Identify the parasite.
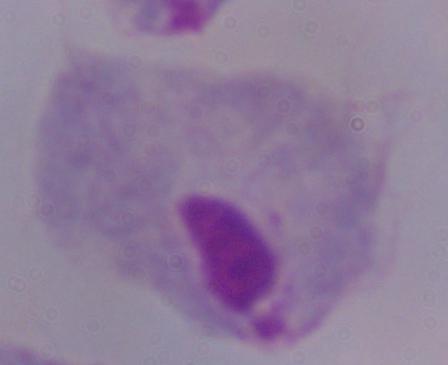
A trichomonad.

Photomicrograph. Captured at 1000x magnification.